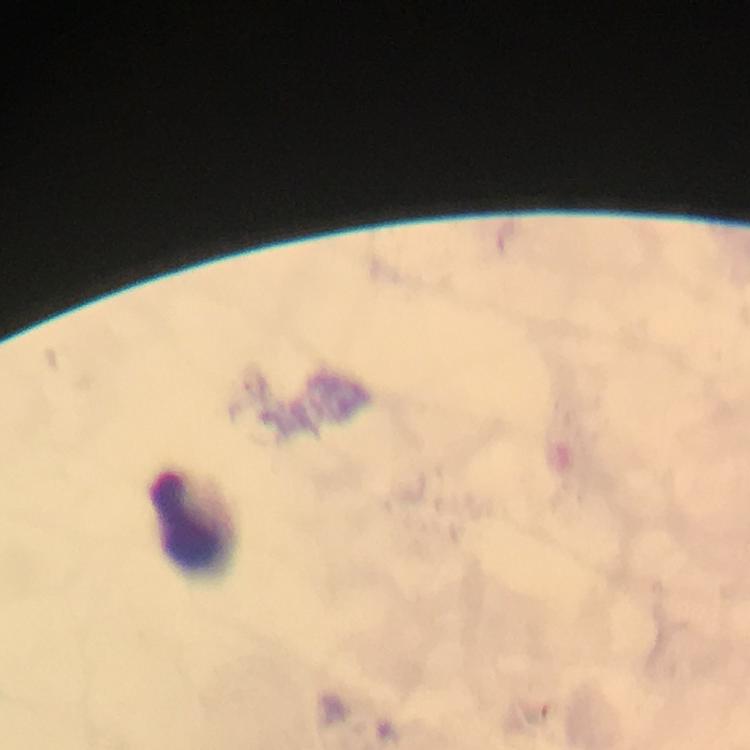
capture: smartphone mounted on the microscope
context: from a diagnostic examination for malaria
cropped_from: a single field of view
magnification: 100x
preparation: thick smear
malaria_parasites: none detected
immersion_oil: applied
leukocyte_locations: 'approximate centers as [x, y] in pixels: [190, 519]'
stain: Giemsa
image_size: 750×750 pixels